State which parasite is depicted.
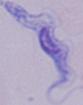

This is a trypanosome.

Micrograph. 1000x magnification.